Assess the morphology of the red blood cells.
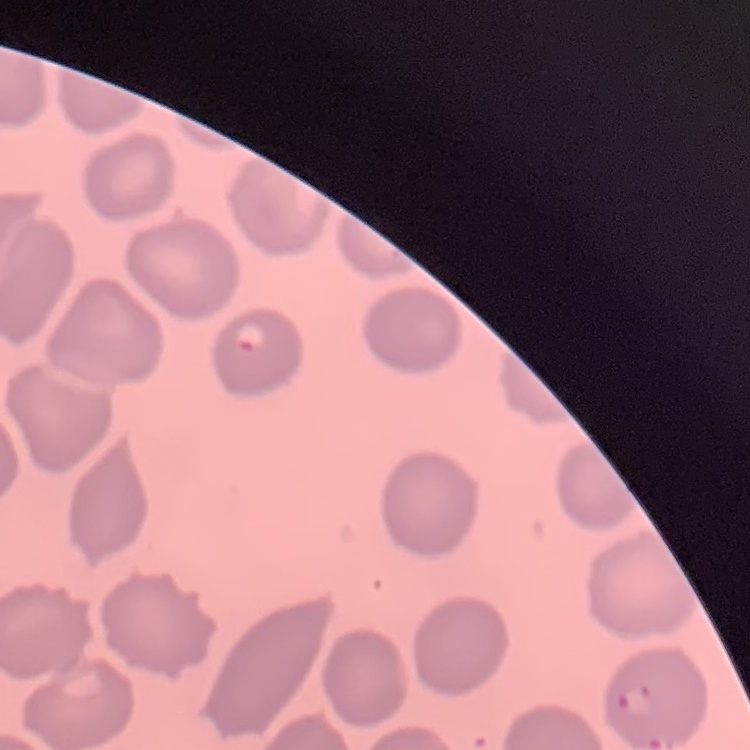
No rouleaux formation.

stain = Field's or Giemsa
preparation = thin peripheral smear
image type = square crop of a larger photomicrograph